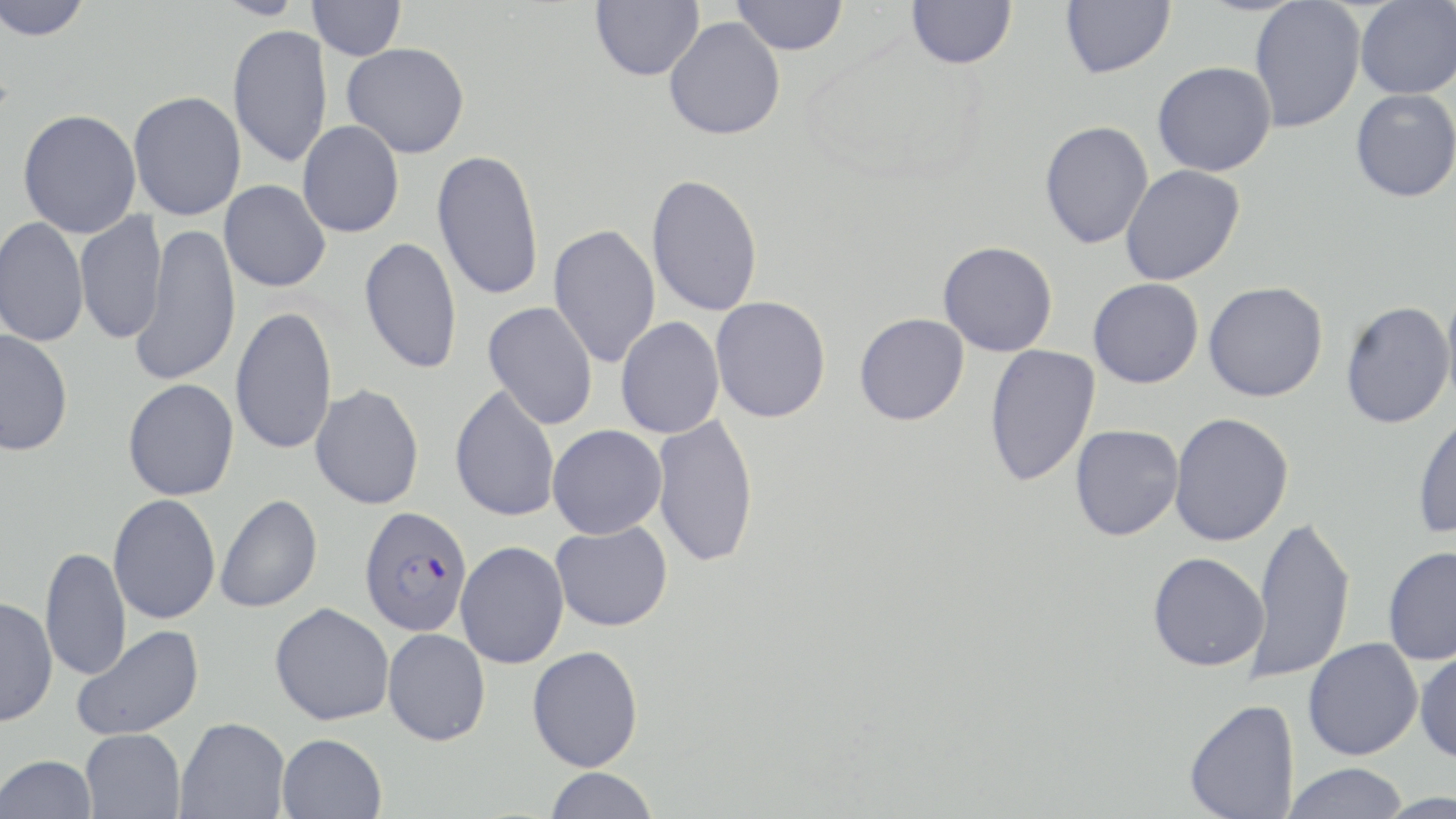

Summary:
  - Coordinate format: approximate bounding boxes as (x1,y1)-(x2,y2) corner pairs in pixels
  - Uninfected red blood cell locations: (0,0)-(94,41), (307,0)-(406,61), (590,0)-(704,81), (731,0)-(849,55), (906,0)-(1017,69), (1060,0)-(1175,78), (1249,0)-(1366,133), (1354,1)-(1456,99), (664,17)-(785,140), (227,24)-(333,168), (342,42)-(470,158), (1152,61)-(1276,176), (1350,88)-(1456,202), (128,90)-(247,221), (17,108)-(141,238), (298,120)-(404,238), (1040,120)-(1153,249), (432,148)-(545,301), (1120,165)-(1245,286), (646,173)-(763,317), (219,180)-(331,293), (74,211)-(167,345), (0,216)-(89,348), (548,223)-(661,368), (131,224)-(241,388), (358,237)-(462,375), (938,241)-(1058,357), (1088,277)-(1204,388), (1203,281)-(1329,402), (1440,285)-(1456,415), (710,296)-(831,423), (483,301)-(598,430), (1341,301)-(1453,429), (230,305)-(337,456), (854,313)-(969,426), (615,316)-(724,439), (0,329)-(73,457), (984,344)-(1100,487), (123,378)-(239,500), (310,383)-(424,510), (450,384)-(560,523), (1413,409)-(1456,539), (1169,412)-(1294,546), (652,413)-(760,568), (1070,424)-(1183,540), (547,425)-(667,539), (108,494)-(221,624), (215,494)-(322,613), (1246,514)-(1356,684), (551,521)-(673,632), (455,541)-(569,669), (1382,546)-(1456,665), (40,547)-(130,682), (1147,551)-(1269,672), (0,596)-(58,727), (270,602)-(394,725), (71,625)-(204,741), (383,628)-(491,746), (1303,638)-(1423,760), (527,645)-(644,771), (1415,646)-(1456,763), (1183,698)-(1299,819), (176,717)-(290,819), (80,728)-(186,818), (275,733)-(387,819), (1,754)-(98,818), (1283,763)-(1409,819), (543,768)-(659,819)
  - Plasmodium falciparum-infected red blood cell locations: (358,505)-(473,637)
  - Slide-level diagnosis: Plasmodium falciparum
  - Modality: light microscopy
  - Field of view: one of a larger specimen
  - Stain: May-Grünwald-Giemsa
  - Preparation: thin blood smear
  - Image size: 1456×819 pixels
  - Magnification: 1000x